Locate platelets.
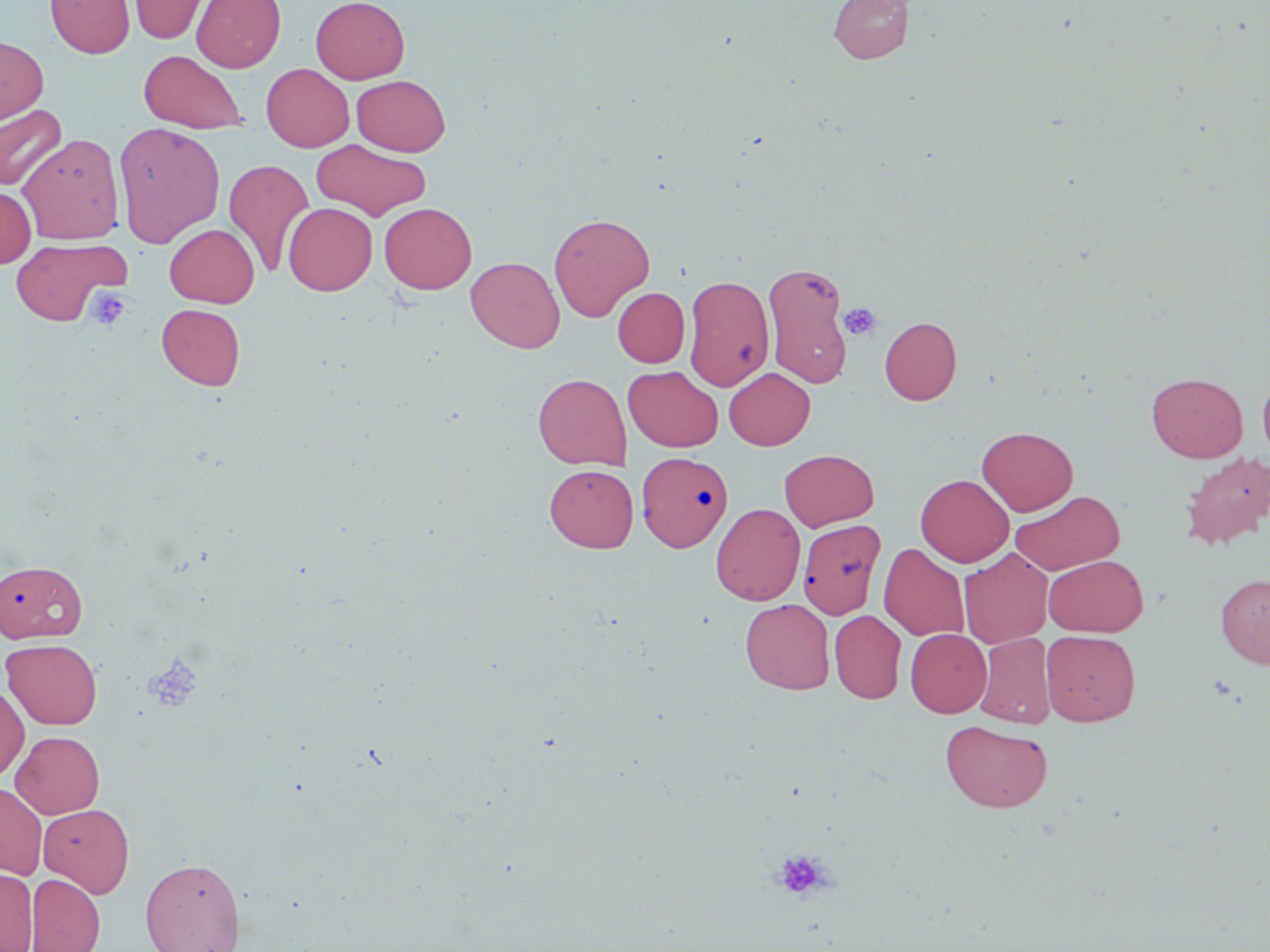

Approximate bounding boxes as (x1, y1, x2, y2) in pixels.
Platelets: (87, 288, 131, 330), (839, 302, 881, 340), (144, 654, 203, 712), (772, 848, 833, 901).

Summary:
  - Uninfected red blood cell locations: (45, 0, 135, 58), (128, 0, 213, 44), (192, 0, 285, 72), (311, 0, 409, 84), (829, 0, 912, 64), (0, 35, 48, 125), (138, 50, 248, 134), (261, 63, 354, 152), (351, 75, 450, 156), (1, 104, 67, 191), (113, 121, 225, 247), (18, 133, 125, 244), (311, 139, 431, 221), (224, 159, 314, 276), (0, 186, 36, 268), (283, 203, 377, 295), (379, 203, 477, 294), (549, 213, 655, 321), (165, 224, 259, 307), (11, 236, 129, 326), (466, 257, 564, 352), (762, 261, 854, 389), (683, 275, 774, 391), (613, 288, 689, 367), (157, 304, 245, 390), (879, 316, 962, 405), (623, 366, 723, 452), (725, 368, 815, 450), (533, 373, 632, 470), (1147, 373, 1247, 462), (1258, 373, 1270, 461), (977, 426, 1077, 516), (779, 449, 879, 531), (1179, 451, 1270, 549), (640, 452, 736, 552), (544, 464, 638, 552), (915, 474, 1013, 566), (1010, 490, 1124, 575), (711, 503, 805, 605), (798, 519, 886, 619), (878, 543, 970, 641), (959, 547, 1053, 648), (1044, 555, 1148, 636), (0, 560, 86, 643), (1216, 574, 1270, 668), (740, 598, 835, 694), (829, 610, 906, 703), (906, 629, 992, 717), (1041, 630, 1140, 726), (974, 633, 1054, 728), (2, 638, 102, 729), (0, 684, 29, 782), (940, 719, 1053, 813), (11, 731, 105, 818), (0, 782, 47, 880), (38, 804, 134, 897), (140, 857, 245, 952), (0, 868, 37, 952), (26, 872, 105, 952)
  - Slide-level diagnosis: no evidence of blood parasites
  - Image size: 1270×952 pixels
  - Preparation: thin blood film
  - Field of view: single
  - Stain: May-Grünwald-Giemsa
  - Magnification: 1000x
  - Modality: light microscopy